Assess this cell for malaria.
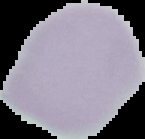

It is uninfected.

Summary:
  - Image type: segmented cell region on a black background
  - Preparation: thin blood film
  - Image size: 145×139 pixels